Give the position of every leukocyte visible.
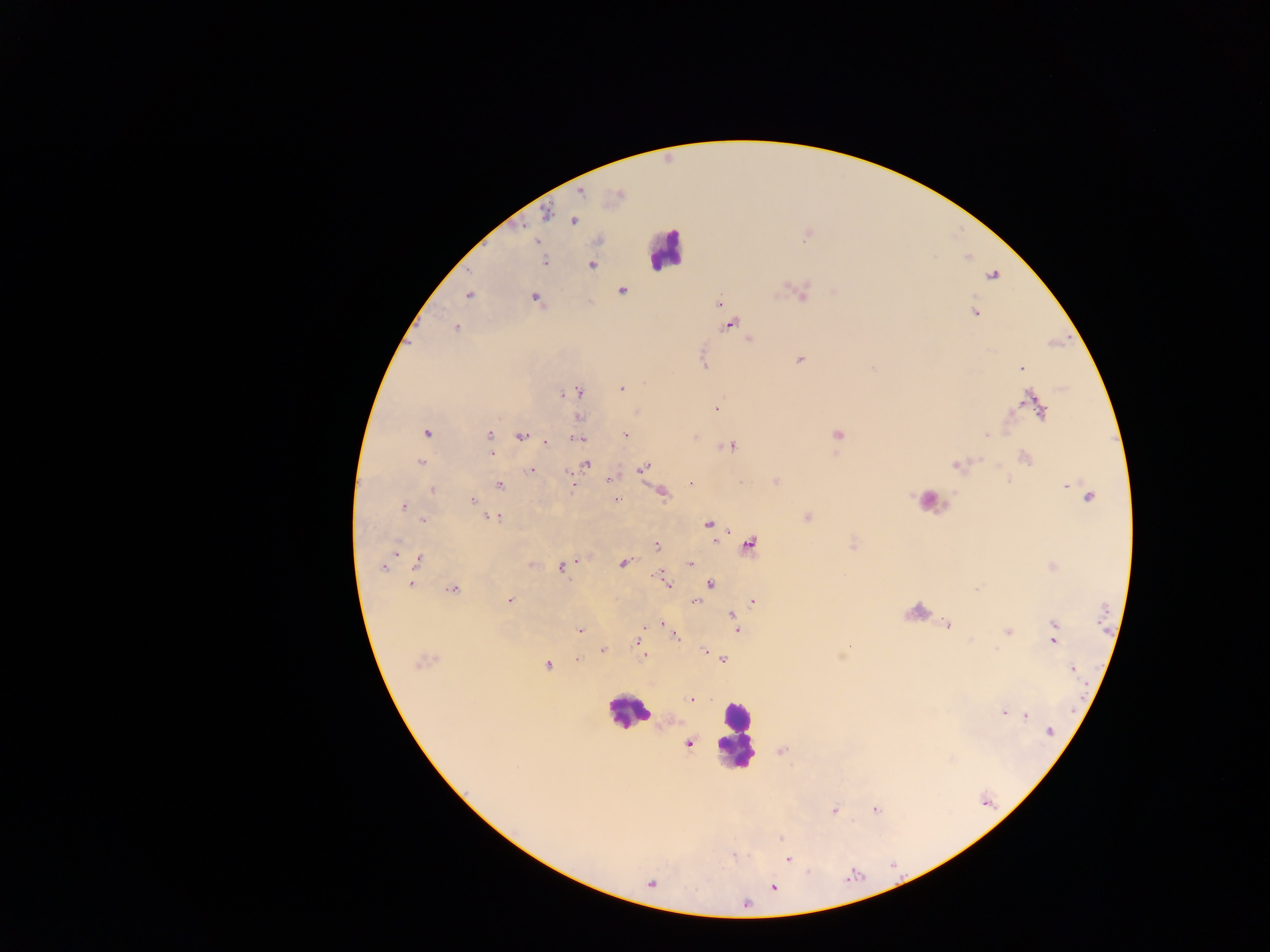

Approximate centers as (x, y) in pixels.
Leukocytes: (666, 250), (931, 500), (919, 611), (628, 712), (736, 734).

Summary:
  - Malaria parasite locations: (581, 193), (546, 212), (573, 221), (544, 261), (592, 265), (992, 275), (622, 290), (802, 292), (469, 294), (535, 298), (718, 302), (975, 312), (730, 325), (456, 327), (749, 339), (800, 359), (1021, 367), (621, 388), (578, 392), (563, 394), (1034, 403), (716, 409), (1040, 410), (425, 432), (625, 435), (488, 436), (522, 436), (838, 436), (986, 436), (577, 438), (546, 441), (732, 446), (491, 452), (1025, 459), (422, 462), (586, 463), (956, 465), (643, 468), (532, 470), (610, 480), (776, 482), (691, 483), (499, 485), (572, 485), (1068, 487), (432, 490), (662, 493), (1088, 497), (616, 499), (471, 500), (403, 507), (807, 516), (492, 517), (423, 521), (709, 524), (657, 545), (750, 545), (418, 560), (623, 563), (690, 563), (533, 564), (568, 564), (563, 566), (383, 567), (659, 576), (666, 582), (711, 584), (411, 585), (452, 588), (509, 601), (695, 601), (753, 601), (733, 615), (736, 623), (662, 624), (948, 625), (737, 630), (579, 631), (1007, 631), (674, 635), (1055, 635), (639, 636), (638, 644), (603, 651), (705, 651), (644, 655), (578, 658), (723, 659), (423, 662), (547, 666), (1072, 668), (692, 699), (1003, 713), (1026, 716), (1051, 732), (689, 744), (834, 810), (875, 810), (781, 839), (788, 859), (774, 887), (745, 904)
  - Image size: 1270×952 pixels
  - Preparation: thick blood film
  - Country: Ghana
  - Capture: mobile-phone photograph through a microscope
  - Field of view: single